Classify this cell by malaria status.
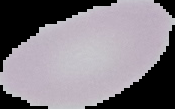

Uninfected.

Image is 175×109 pixels. From a thin blood film. Cell region segmented out of the field of view; the surrounding area is masked to black.